Report the malaria status of this cell.
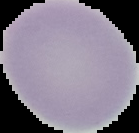

Uninfected.

{
  "preparation": "thin blood smear",
  "image_type": "segmented cell region on a black background",
  "image_size": "139×133 pixels"
}